State which parasite is depicted.
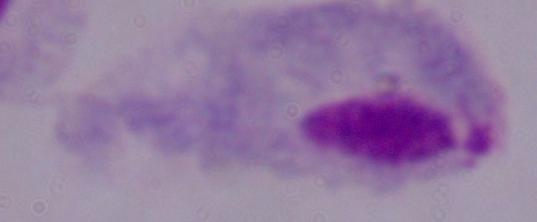
A trichomonad.

modality = micrograph
magnification = 1000x